State which parasite is depicted.
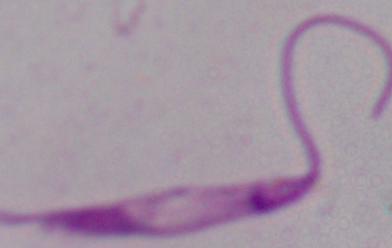
Leishmania.

magnification = 1000x
modality = photomicrograph